Identify the parasite.
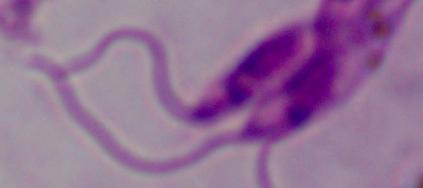
This is Leishmania.

Micrograph. 1000x magnification.